Report the malaria status of this cell.
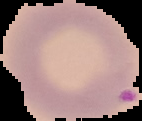
Parasitized.

preparation: thin blood smear
image_type: segmented cell region with the area outside set to black
image_size: 142×121 pixels